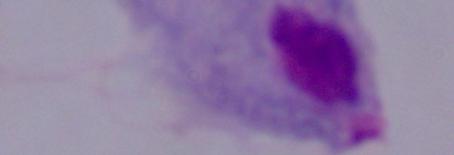

Summary:
  - Identification: trichomonad
  - Modality: micrograph
  - Magnification: 1000x